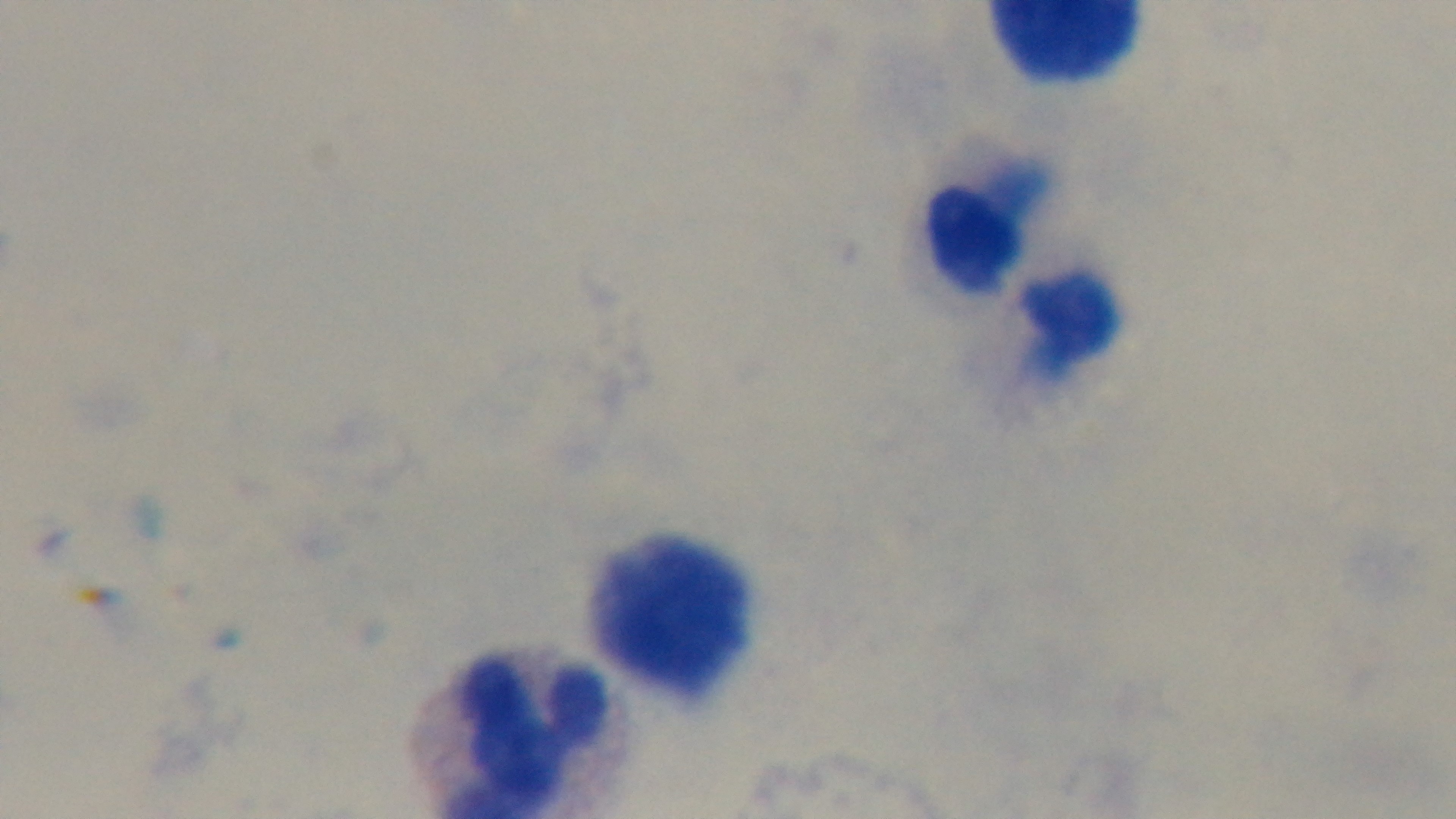
stain = Giemsa
objective = 100x oil immersion
capture = mounted 4K digital camera
preparation = thick blood film
modality = light microscopy
malaria status = uninfected
field of view = single